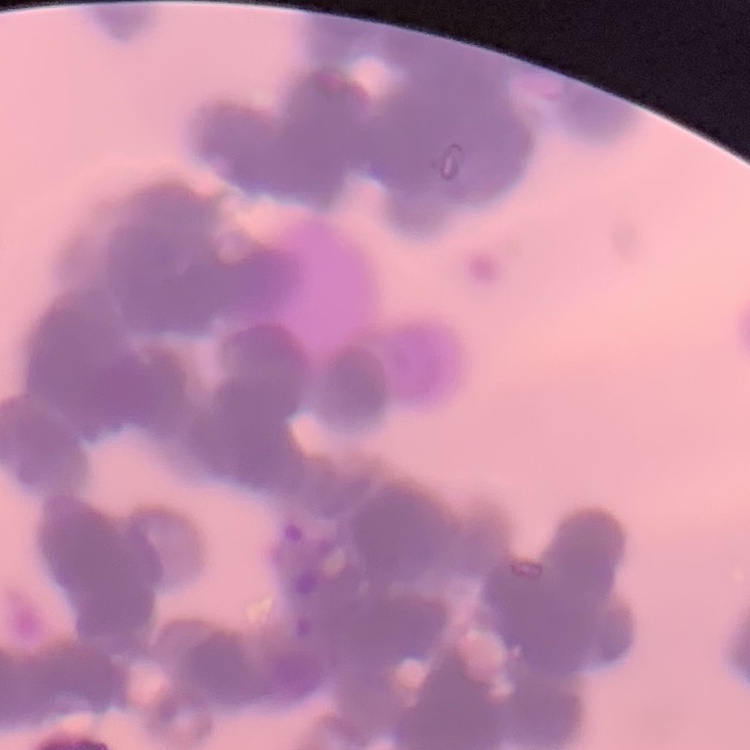

erythrocyte morphology = rouleaux formation
image type = square crop of a larger photomicrograph
preparation = thin blood smear
stain = Field's or Giemsa